Report the malaria status of this cell.
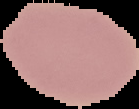

It is uninfected.

{
  "image_size": "139×109 pixels",
  "image_type": "segmented cell region with the area outside set to black",
  "preparation": "thin blood smear"
}